Name the parasite shown.
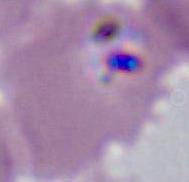
This is Plasmodium.

Micrograph. 400x or 1000x magnification.